Assess this cell for malaria.
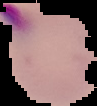
It is parasitized.

Summary:
  - Image type: segmented cell region on a black background
  - Image size: 97×106 pixels
  - Preparation: thin blood smear